Classify this cell by malaria status.
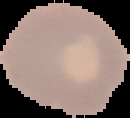
It is uninfected.

{
  "image_type": "cell region segmented out of the field of view; surrounding area masked to black",
  "image_size": "130×118 pixels",
  "preparation": "thin blood film"
}